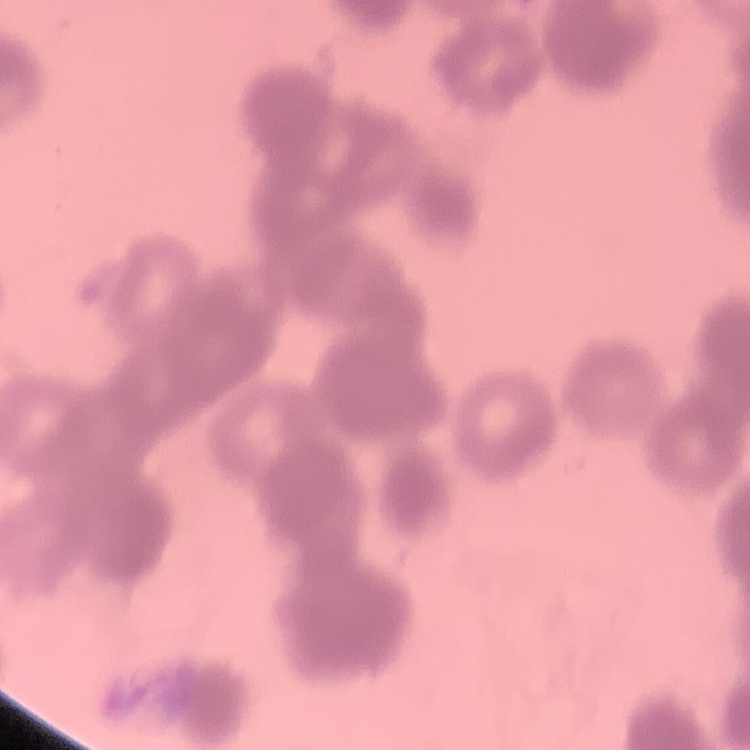
Summary:
  - Red blood cell morphology: rouleaux formation
  - Stain: Field's or Giemsa
  - Image type: square crop of a larger photomicrograph
  - Preparation: thin blood smear